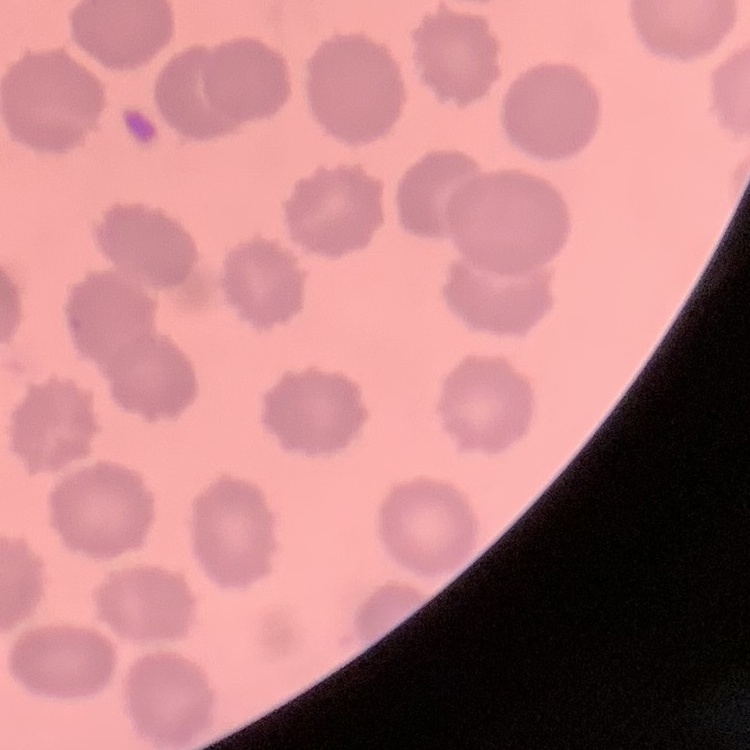 The red blood cells show no rouleaux formation. Thin blood smear. One tile cut from a larger photomicrograph. Stained with either Field's or Giemsa.